Name the parasite shown.
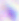

This is Toxoplasma gondii.

Micrograph. Captured at 400x magnification.